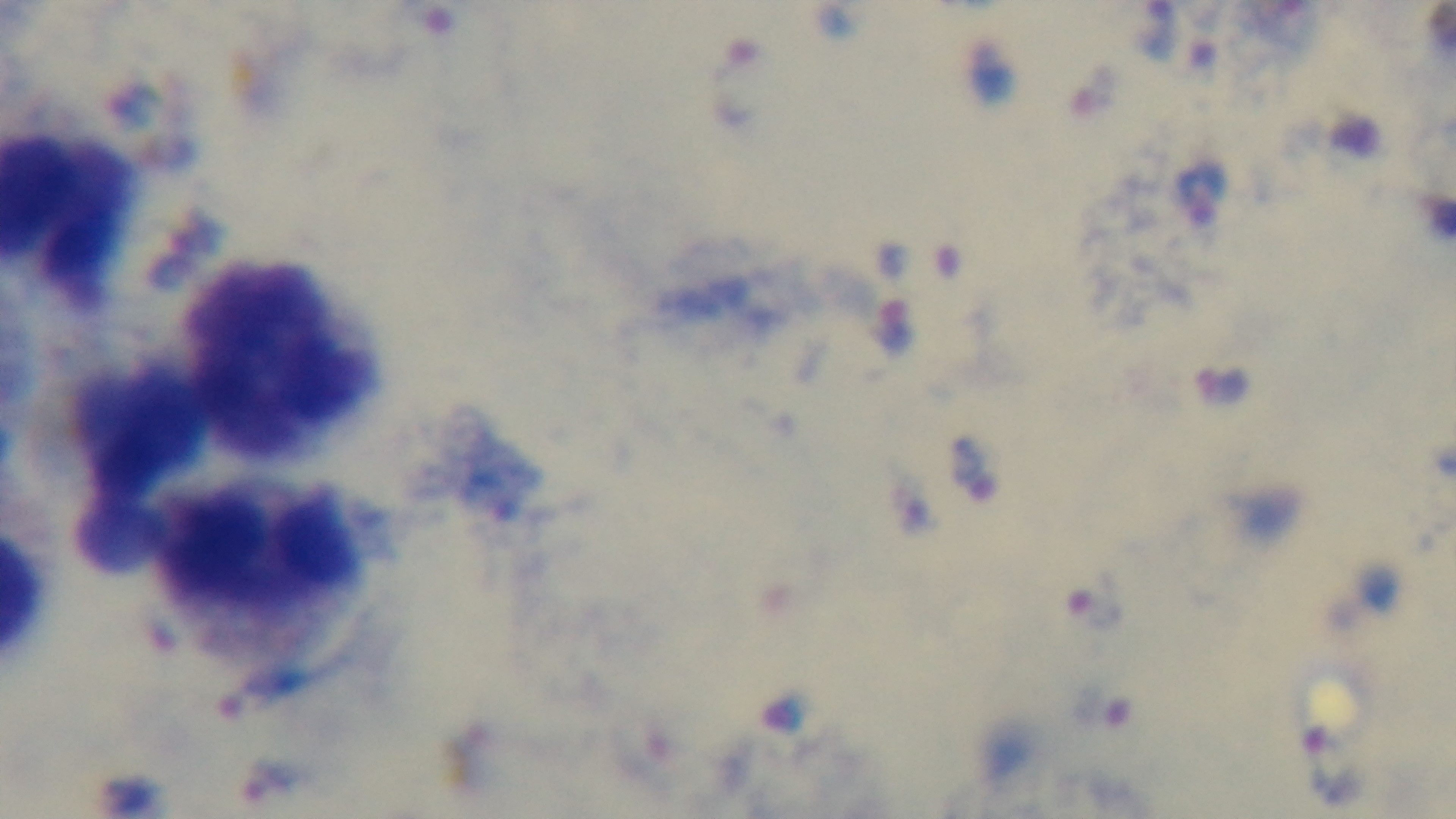

Summary:
  - Capture: mounted 4K digital camera
  - Malaria status: infected
  - Objective: 100x oil immersion
  - Preparation: thick blood film
  - Modality: light microscopy
  - Stain: Giemsa
  - Field of view: single